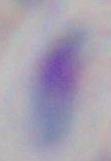 1000x magnification. Toxoplasma gondii is seen. Micrograph.